Give the position of every leukocyte visible.
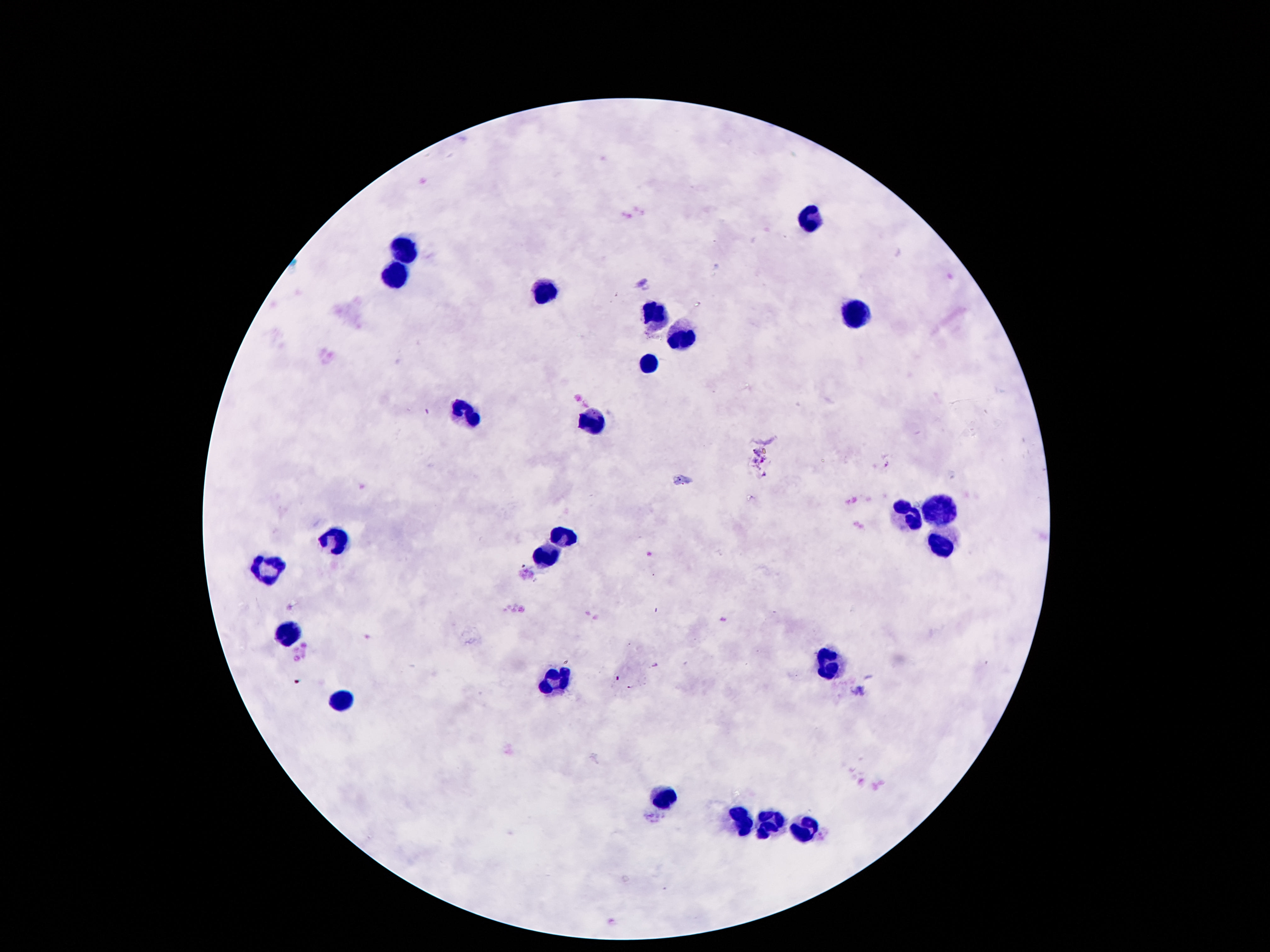

Approximate centers as (x, y) in pixels.
Leukocytes: (810, 220), (406, 247), (400, 275), (539, 291), (656, 313), (850, 322), (677, 338), (645, 363), (465, 417), (589, 422), (903, 513), (934, 513), (567, 536), (334, 543), (945, 548), (546, 557), (264, 569), (290, 635), (833, 666), (551, 681), (337, 702), (663, 796), (747, 821), (773, 821), (805, 828).

image_size: 1270×952 pixels
capture: smartphone camera through the microscope eyepiece
patient_malaria_status: uninfected
stain: Giemsa
magnification: 100x
preparation: thick blood film
field_of_view: one from this slide